Report the malaria status of this cell.
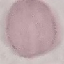
Uninfected.

Acquired by smartphone through the microscope eyepiece. Thin blood film. Giemsa-stained preparation. Automatically extracted cell patch, resized to 64 × 64 pixels.